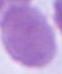
{
  "identification": "erythrocyte",
  "magnification": "1000x",
  "modality": "photomicrograph"
}